Assess this cell for malaria.
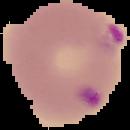
It is parasitized.

From a thin blood smear. Segmented cell region on a black background. Image is 130×130 pixels.